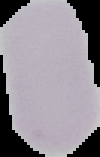
image size = 100×157 pixels
image type = cell region segmented out of the field of view; surrounding area masked to black
malaria status = uninfected
preparation = thin blood smear